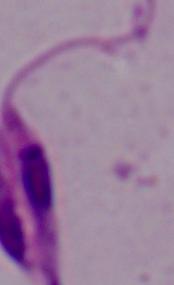

identification = Leishmania
magnification = 1000x
modality = photomicrograph